Locate every Plasmodium parasite.
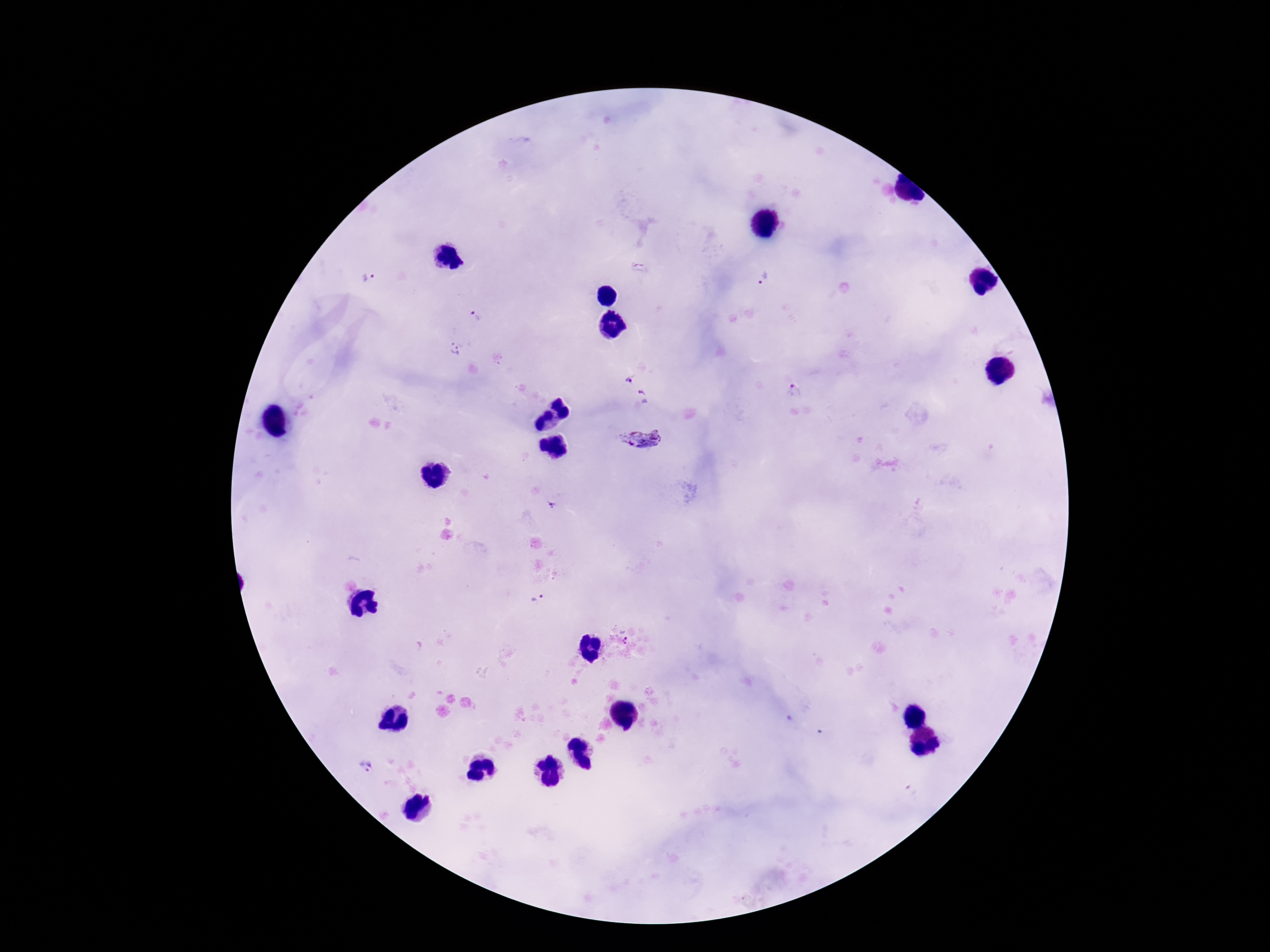
Approximate centers as [x, y] in pixels.
Plasmodium parasites: [640, 268], [763, 276], [369, 281], [477, 317], [455, 350], [629, 380], [794, 390], [643, 397], [642, 438], [535, 598], [365, 766].

Giemsa-stained preparation. One field from this slide. Patient malaria status: infected. Image is 1270×952 pixels. Thick blood smear. 100x magnification. Smartphone photograph taken through the microscope eyepiece.